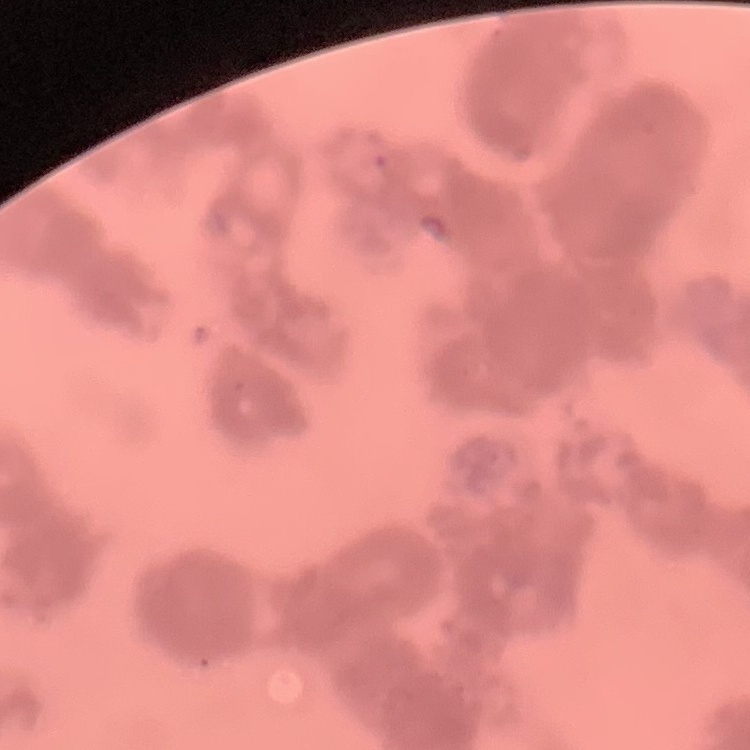
red blood cell morphology = rouleaux formation
image type = one tile cut from a larger photomicrograph
stain = Field's or Giemsa
preparation = thin peripheral smear